Describe the morphology of the erythrocytes.
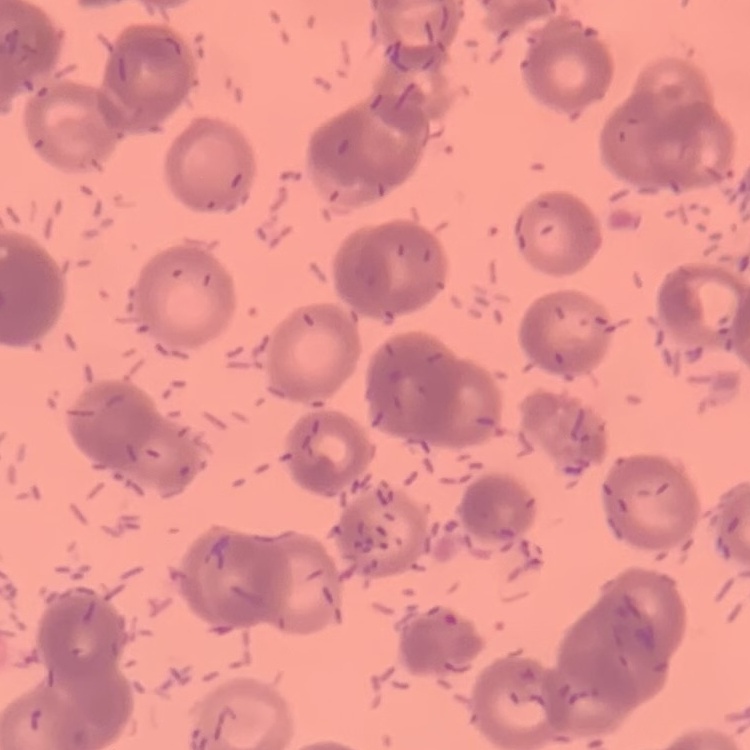
They show rouleaux formation.

Thin blood film. Stained with either Field's or Giemsa. Square crop of a larger photomicrograph.